Classify this cell by malaria status.
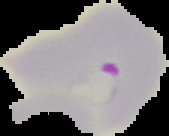

Parasitized.

Image is 169×136 pixels. Segmented cell region on a black background. From a thin blood film.